Outline platelets.
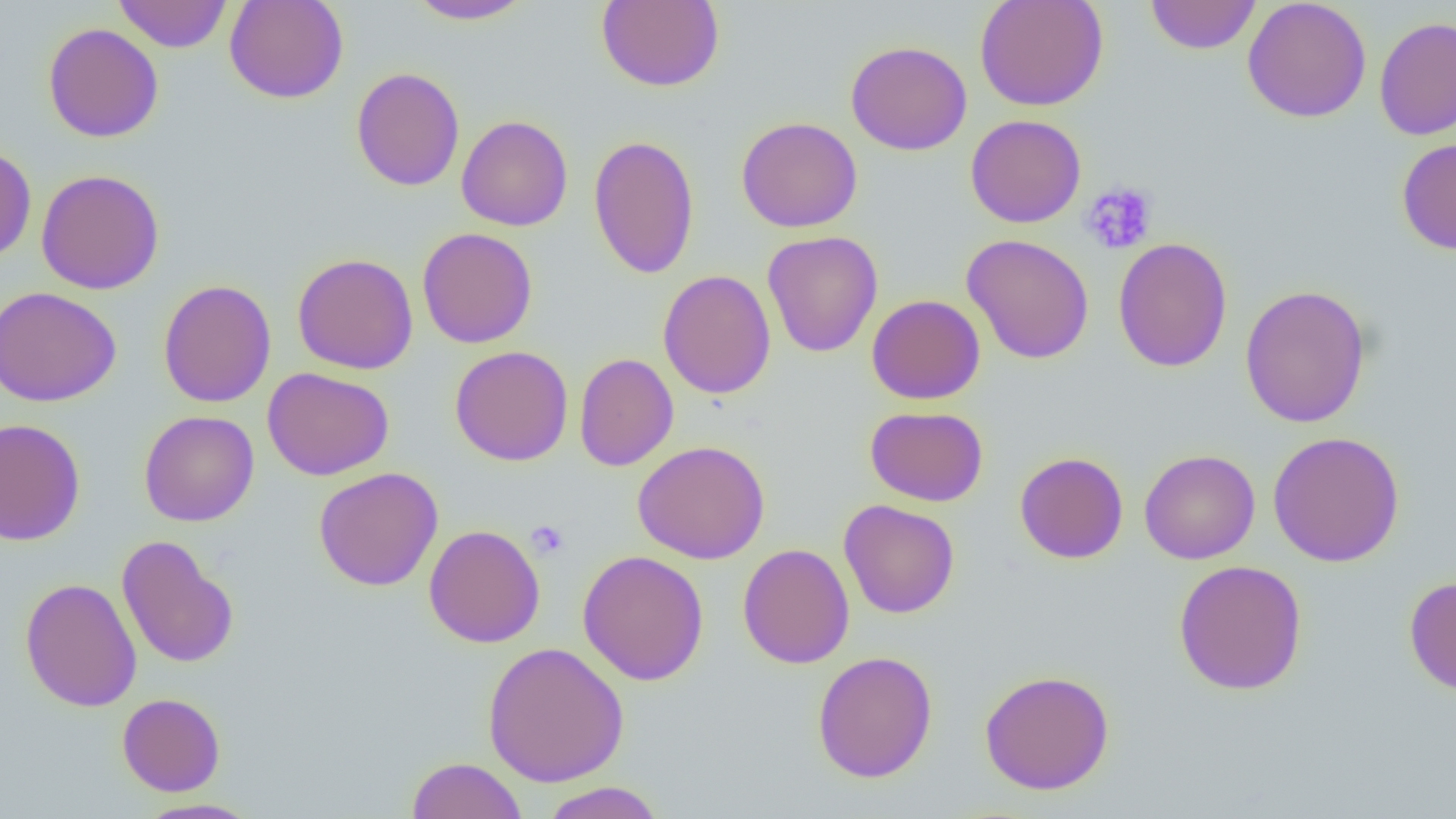

Approximate bounding boxes as named x1/y1/x2/y2 corners in pixels.
Platelets: (x1=1080, y1=182, x2=1158, y2=255), (x1=526, y1=520, x2=570, y2=560).

slide-level diagnosis = no evidence of blood parasites
field of view = single
preparation = thin blood smear
magnification = 1000x
uninfected red blood cell locations = approximate bounding boxes as named x1/y1/x2/y2 corners in pixels: (x1=113, y1=0, x2=232, y2=53), (x1=224, y1=0, x2=349, y2=104), (x1=596, y1=0, x2=725, y2=92), (x1=975, y1=0, x2=1108, y2=111), (x1=1145, y1=0, x2=1261, y2=55), (x1=406, y1=1, x2=536, y2=25), (x1=1242, y1=1, x2=1372, y2=123), (x1=1373, y1=16, x2=1456, y2=141), (x1=43, y1=23, x2=164, y2=143), (x1=846, y1=40, x2=972, y2=155), (x1=351, y1=67, x2=465, y2=191), (x1=456, y1=115, x2=573, y2=231), (x1=965, y1=115, x2=1086, y2=228), (x1=736, y1=116, x2=863, y2=233), (x1=588, y1=135, x2=700, y2=280), (x1=1396, y1=137, x2=1456, y2=255), (x1=0, y1=145, x2=36, y2=263), (x1=36, y1=169, x2=165, y2=294), (x1=417, y1=227, x2=537, y2=349), (x1=762, y1=230, x2=883, y2=358), (x1=961, y1=233, x2=1095, y2=365), (x1=1113, y1=237, x2=1233, y2=372), (x1=292, y1=252, x2=419, y2=374), (x1=658, y1=269, x2=776, y2=399), (x1=157, y1=279, x2=277, y2=407), (x1=1240, y1=284, x2=1371, y2=428), (x1=0, y1=286, x2=122, y2=407), (x1=866, y1=295, x2=985, y2=405), (x1=449, y1=346, x2=574, y2=466), (x1=574, y1=353, x2=678, y2=472), (x1=262, y1=367, x2=394, y2=481), (x1=865, y1=405, x2=989, y2=506), (x1=139, y1=410, x2=260, y2=527), (x1=0, y1=417, x2=86, y2=546), (x1=1267, y1=431, x2=1405, y2=567), (x1=632, y1=440, x2=770, y2=564), (x1=1139, y1=448, x2=1261, y2=564), (x1=1014, y1=451, x2=1129, y2=564), (x1=313, y1=467, x2=444, y2=591), (x1=838, y1=499, x2=960, y2=619), (x1=424, y1=524, x2=545, y2=648), (x1=116, y1=535, x2=239, y2=669), (x1=738, y1=543, x2=855, y2=669), (x1=577, y1=550, x2=709, y2=686), (x1=1173, y1=559, x2=1308, y2=695), (x1=1404, y1=575, x2=1456, y2=697), (x1=20, y1=577, x2=141, y2=712), (x1=482, y1=641, x2=630, y2=787), (x1=812, y1=650, x2=939, y2=783), (x1=979, y1=669, x2=1115, y2=795), (x1=117, y1=693, x2=226, y2=796), (x1=406, y1=757, x2=528, y2=819), (x1=539, y1=781, x2=666, y2=819), (x1=135, y1=797, x2=263, y2=818)
image size = 1456×819 pixels
modality = light microscopy